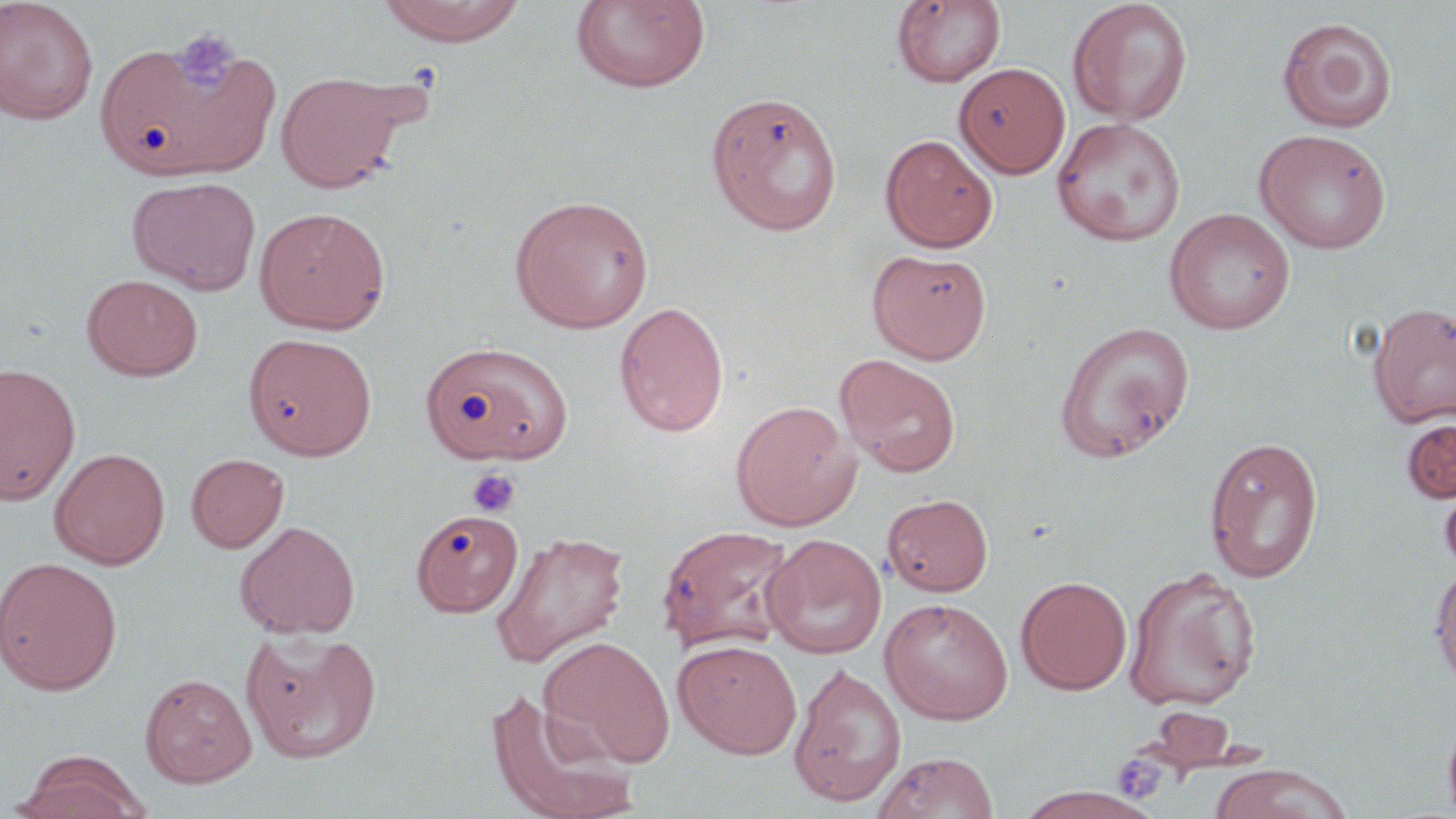
Summary:
  - Coordinate format: approximate bounding boxes as (x1, y1, x2, y2) in pixels
  - Platelet locations: (172, 29, 239, 94), (465, 467, 521, 518), (1111, 754, 1166, 802)
  - Uninfected red blood cell locations: (1067, 0, 1192, 125), (0, 1, 98, 125), (375, 1, 528, 46), (569, 1, 711, 93), (891, 1, 1007, 89), (1277, 17, 1397, 134), (95, 34, 276, 180), (954, 62, 1071, 178), (276, 71, 406, 193), (704, 92, 843, 235), (1051, 117, 1186, 247), (1255, 129, 1392, 254), (880, 134, 998, 252), (127, 176, 261, 295), (509, 194, 653, 333), (254, 206, 391, 334), (1164, 208, 1296, 335), (867, 248, 991, 364), (82, 274, 203, 380), (613, 301, 730, 437), (1367, 301, 1456, 429), (1054, 321, 1196, 463), (244, 332, 378, 460), (420, 341, 572, 465), (835, 354, 961, 477), (0, 363, 81, 505), (730, 400, 860, 531), (1401, 418, 1456, 503), (1204, 436, 1323, 583), (50, 447, 170, 569), (186, 453, 289, 553), (1440, 475, 1456, 578), (883, 494, 993, 596), (412, 509, 524, 617), (234, 521, 361, 639), (656, 524, 796, 654), (490, 530, 629, 668), (763, 534, 887, 659), (0, 556, 122, 695), (1430, 563, 1456, 686), (1124, 565, 1262, 711), (1016, 575, 1132, 694), (879, 597, 1014, 725), (241, 629, 383, 764), (539, 636, 675, 766), (673, 639, 802, 759), (789, 663, 906, 808), (140, 673, 256, 787), (485, 689, 639, 819), (1442, 707, 1456, 819), (871, 752, 999, 819), (11, 755, 150, 819), (1209, 764, 1353, 818), (1016, 787, 1162, 819)
  - Slide-level diagnosis: no evidence of blood parasites
  - Stain: May-Grünwald-Giemsa
  - Field of view: one of a larger specimen
  - Image size: 1456×819 pixels
  - Modality: optical microscopy
  - Preparation: thin blood film
  - Magnification: 1000x